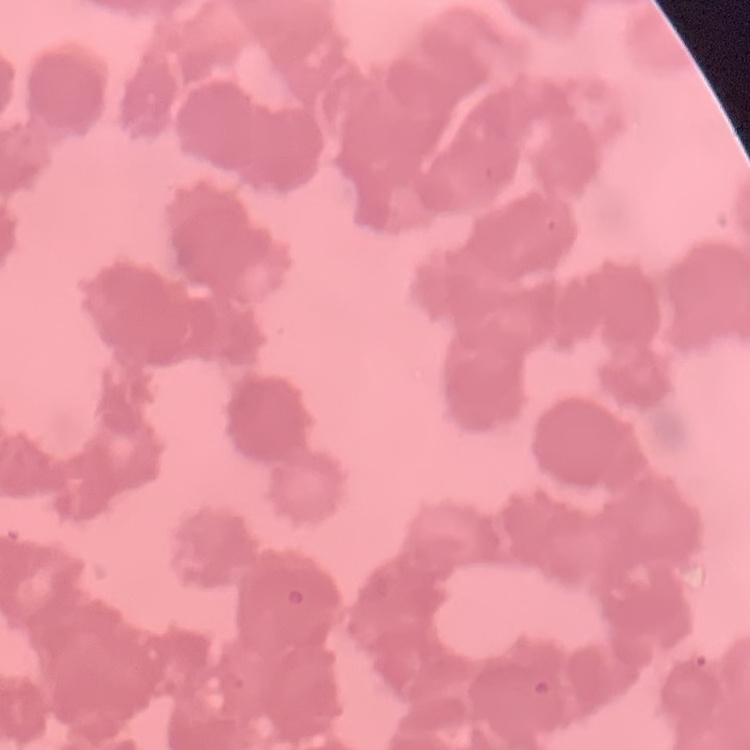

erythrocyte_morphology: rouleaux formation
image_type: square crop of a larger photomicrograph
preparation: thin blood film
stain: Field's or Giemsa